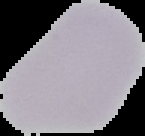
Summary:
  - Preparation: thin blood film
  - Image size: 145×136 pixels
  - Result: negative for Plasmodium parasites
  - Image type: segmented cell region with the area outside set to black